Assess the morphology of the erythrocytes.
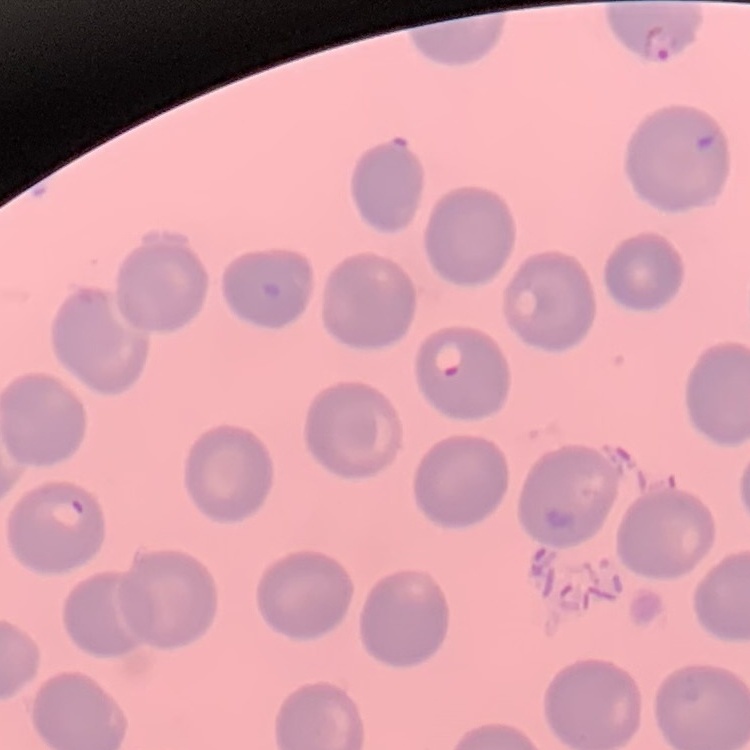
No rouleaux formation.

preparation = thin blood smear
stain = Field's or Giemsa
image type = square crop of a larger photomicrograph